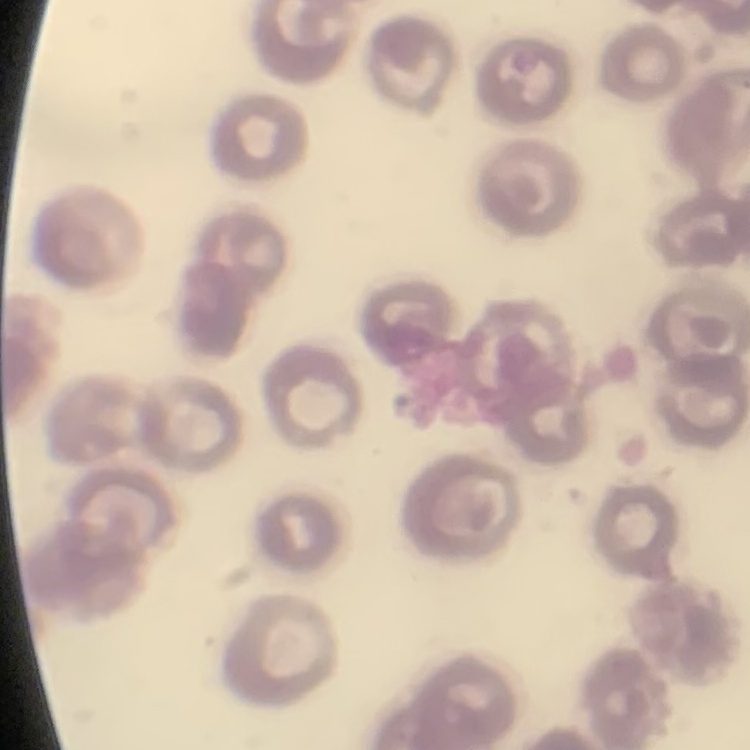
Summary:
  - Erythrocyte morphology: no rouleaux formation
  - Stain: Field's or Giemsa
  - Image type: one tile cut from a larger photomicrograph
  - Preparation: thin peripheral smear